Identify the preparation type.
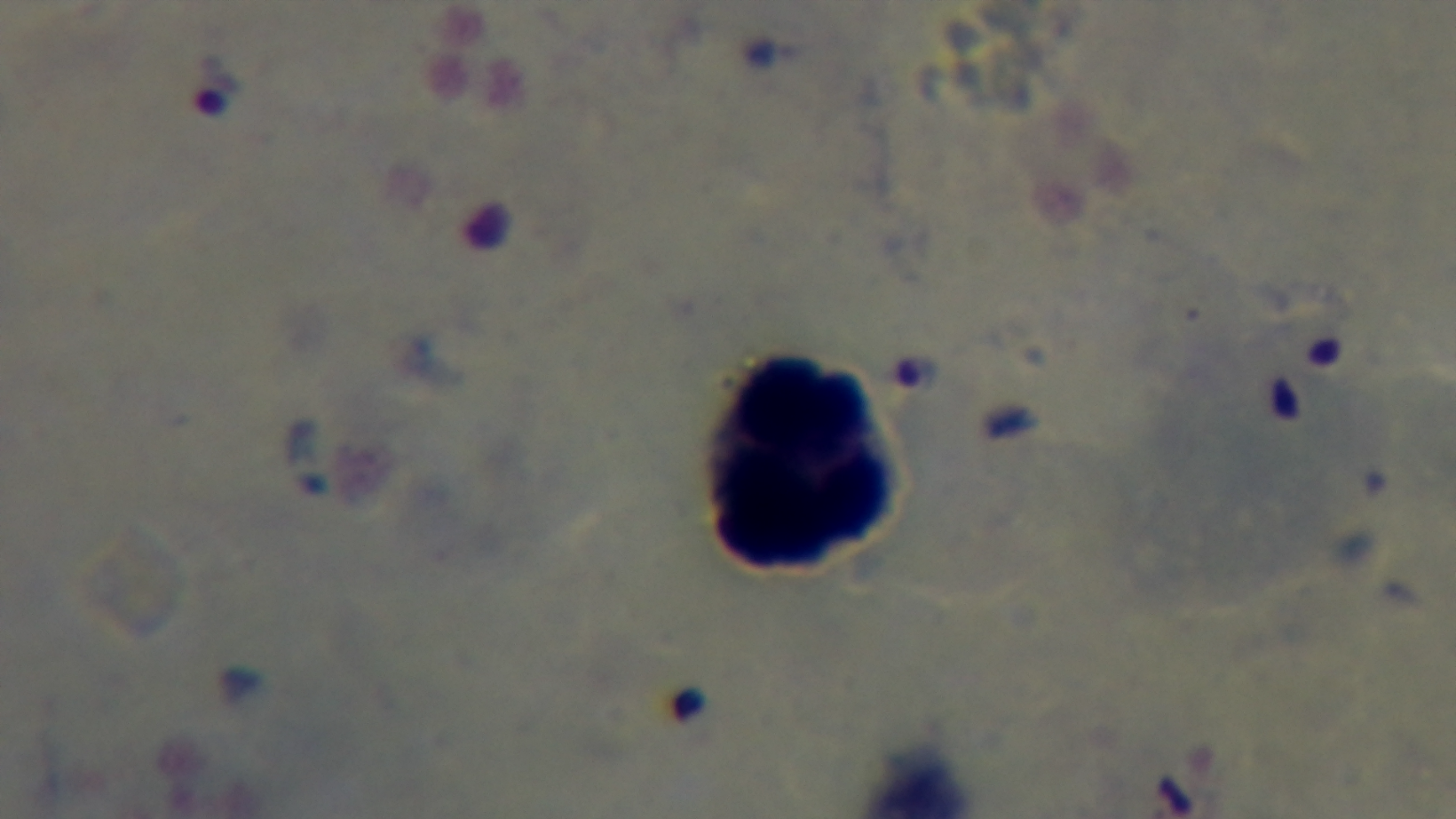

A thick smear.

Mounted 4K digital camera. Oil-immersion objective, 100x. Single field of view. Malaria status: infected. Giemsa stain. Light microscopy.